Report the malaria status of this cell.
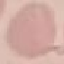
Uninfected.

Summary:
  - Preparation: thin blood smear
  - Image type: automatically extracted cell patch, resized to 64 × 64 pixels
  - Capture: smartphone camera at the microscope eyepiece
  - Stain: Giemsa